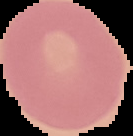 Cell region segmented out of the field of view; the surrounding area is masked to black. Image is 133×136 pixels. Result: no Plasmodium parasites detected. From a thin blood film.